State the blood parasite species.
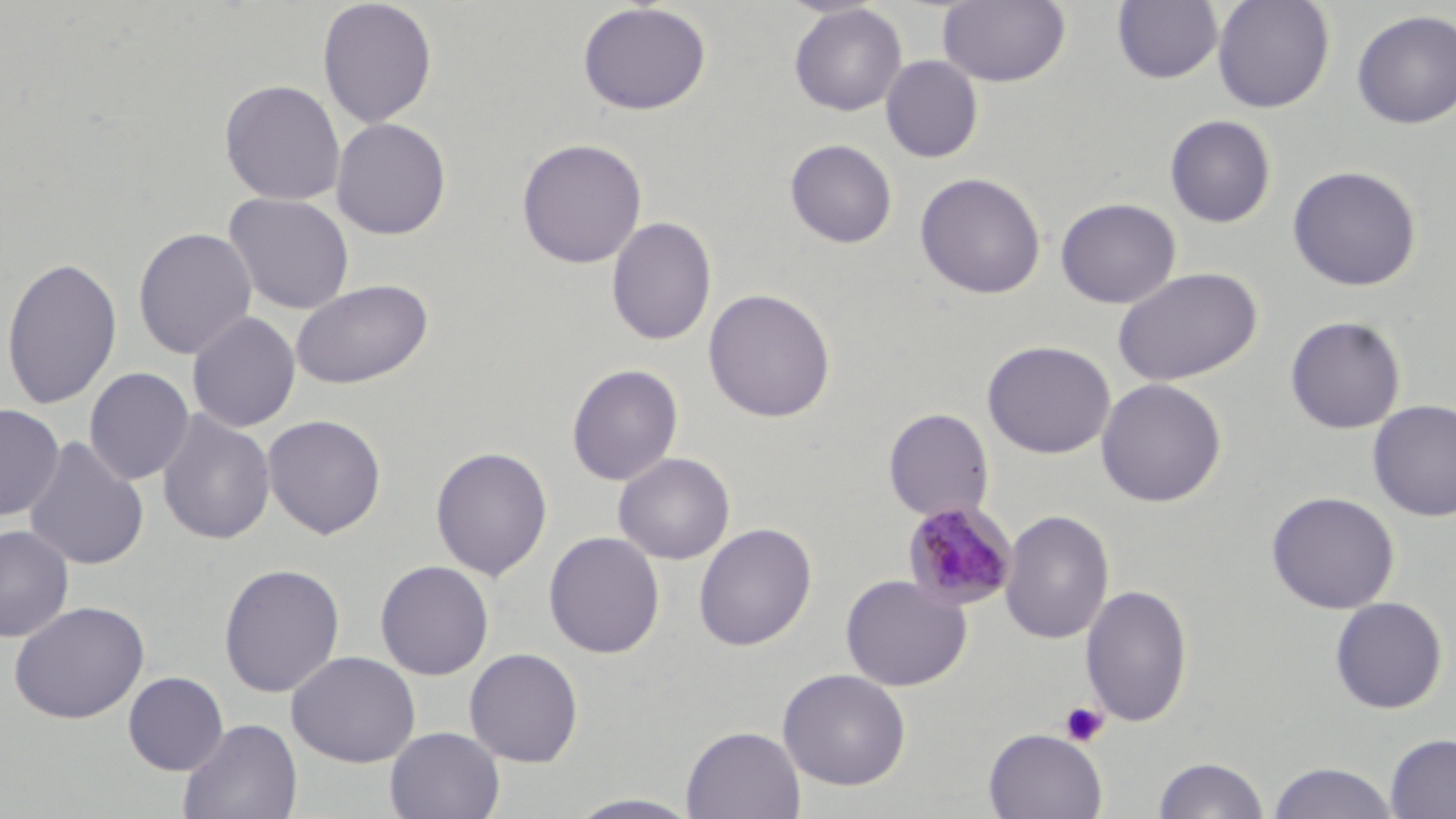
Plasmodium malariae.

image size = 1456×819 pixels
preparation = thin blood film
magnification = 1000x
modality = optical microscopy
platelet locations = approximate bounding boxes as named x1/y1/x2/y2 corners in pixels: (x1=1059, y1=701, x2=1109, y2=746)
field of view = single
uninfected red blood cell locations = approximate bounding boxes as named x1/y1/x2/y2 corners in pixels: (x1=316, y1=0, x2=438, y2=128), (x1=937, y1=0, x2=1070, y2=87), (x1=1212, y1=0, x2=1335, y2=113), (x1=1112, y1=1, x2=1223, y2=84), (x1=577, y1=2, x2=711, y2=116), (x1=789, y1=4, x2=907, y2=116), (x1=1351, y1=10, x2=1456, y2=128), (x1=881, y1=56, x2=983, y2=163), (x1=219, y1=79, x2=346, y2=205), (x1=1164, y1=114, x2=1276, y2=228), (x1=331, y1=117, x2=452, y2=240), (x1=516, y1=137, x2=648, y2=269), (x1=785, y1=138, x2=898, y2=249), (x1=1287, y1=165, x2=1422, y2=291), (x1=914, y1=172, x2=1047, y2=299), (x1=223, y1=192, x2=355, y2=315), (x1=1055, y1=197, x2=1181, y2=308), (x1=606, y1=216, x2=717, y2=347), (x1=133, y1=226, x2=257, y2=360), (x1=1, y1=255, x2=122, y2=410), (x1=1112, y1=267, x2=1262, y2=386), (x1=290, y1=278, x2=433, y2=390), (x1=703, y1=287, x2=836, y2=423), (x1=187, y1=311, x2=301, y2=432), (x1=1285, y1=316, x2=1406, y2=434), (x1=982, y1=340, x2=1116, y2=459), (x1=566, y1=363, x2=684, y2=486), (x1=84, y1=367, x2=194, y2=486), (x1=1094, y1=378, x2=1227, y2=507), (x1=1368, y1=400, x2=1456, y2=521), (x1=0, y1=404, x2=64, y2=521), (x1=883, y1=408, x2=994, y2=521), (x1=156, y1=410, x2=275, y2=545), (x1=262, y1=414, x2=387, y2=540), (x1=23, y1=436, x2=149, y2=571), (x1=430, y1=445, x2=553, y2=582), (x1=613, y1=452, x2=735, y2=565), (x1=1265, y1=491, x2=1400, y2=614), (x1=999, y1=509, x2=1115, y2=645), (x1=694, y1=522, x2=817, y2=651), (x1=0, y1=524, x2=74, y2=643), (x1=544, y1=531, x2=665, y2=659), (x1=374, y1=560, x2=494, y2=680), (x1=218, y1=563, x2=345, y2=698), (x1=839, y1=574, x2=973, y2=691), (x1=1080, y1=584, x2=1193, y2=727), (x1=1329, y1=597, x2=1447, y2=714), (x1=9, y1=600, x2=150, y2=724), (x1=464, y1=647, x2=583, y2=767), (x1=286, y1=650, x2=421, y2=767), (x1=777, y1=667, x2=912, y2=791), (x1=123, y1=671, x2=229, y2=775), (x1=178, y1=717, x2=303, y2=819), (x1=681, y1=725, x2=806, y2=818), (x1=385, y1=727, x2=505, y2=819), (x1=983, y1=728, x2=1107, y2=818), (x1=1384, y1=733, x2=1456, y2=818), (x1=1152, y1=756, x2=1270, y2=818), (x1=1267, y1=761, x2=1400, y2=819), (x1=564, y1=793, x2=707, y2=818)
Plasmodium malariae-infected red blood cell locations = approximate bounding boxes as named x1/y1/x2/y2 corners in pixels: (x1=901, y1=500, x2=1017, y2=610)
stain = May-Grünwald-Giemsa